Identify the parasite.
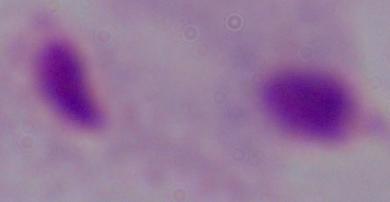

A trichomonad.

1000x magnification. Micrograph.